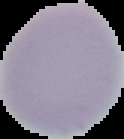

Summary:
  - Preparation: thin blood smear
  - Malaria status: uninfected
  - Image type: segmented cell region on a black background
  - Image size: 124×139 pixels